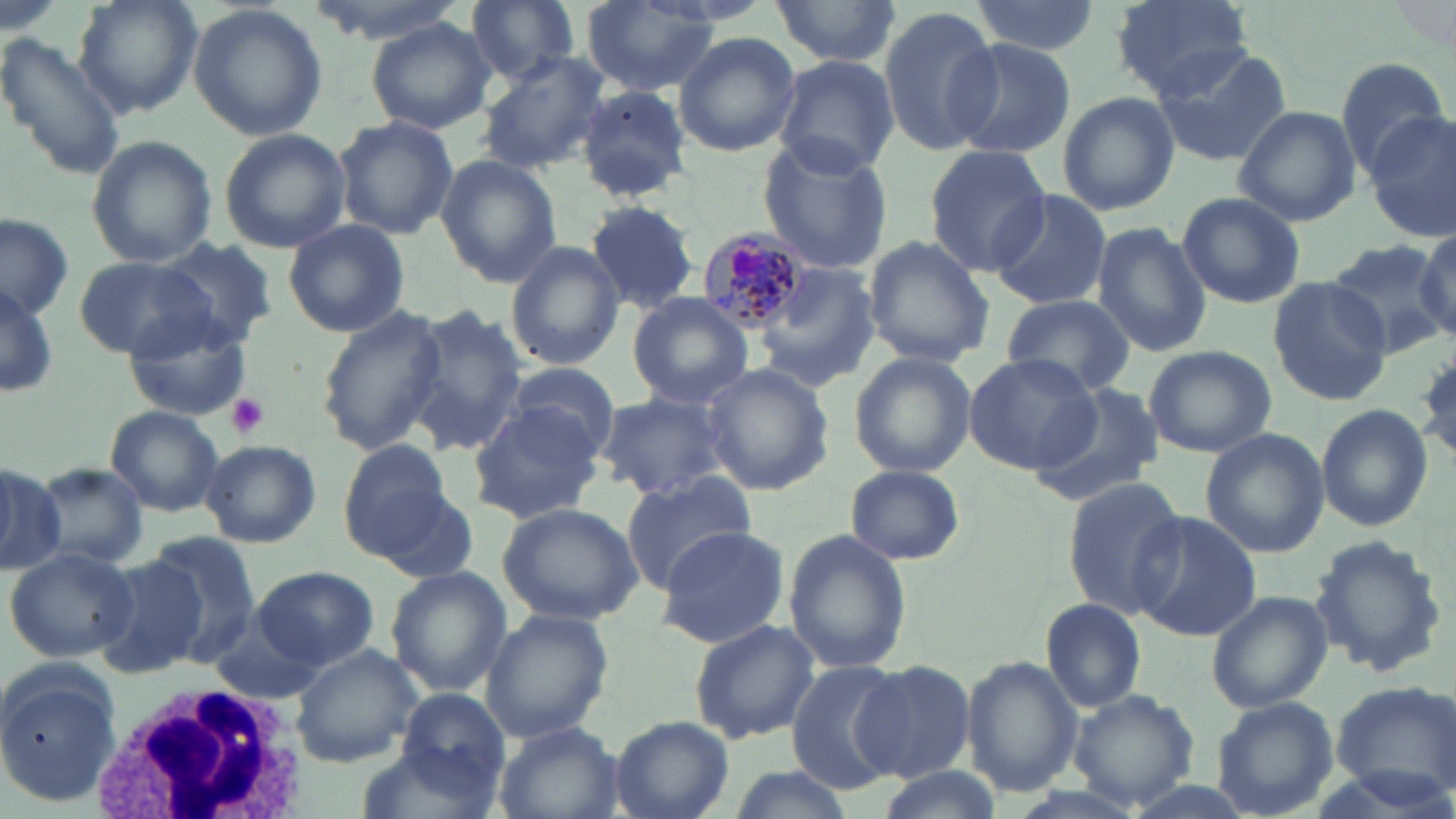
Approximate bounding boxes as [x1, y1, x2, y2] in pixels. Uninfected red blood cell locations: [73, 0, 202, 117], [766, 0, 903, 70], [969, 0, 1100, 56], [1110, 1, 1253, 98], [464, 2, 580, 84], [580, 2, 726, 97], [187, 3, 329, 142], [877, 5, 1000, 157], [366, 18, 496, 135], [0, 32, 127, 179], [672, 32, 801, 158], [943, 37, 1076, 161], [1153, 39, 1289, 169], [478, 45, 609, 177], [771, 55, 900, 178], [1332, 56, 1449, 176], [574, 86, 694, 203], [1058, 92, 1178, 216], [1233, 105, 1361, 226], [1365, 112, 1455, 240], [331, 116, 459, 241], [219, 127, 349, 252], [85, 135, 217, 268], [757, 138, 895, 273], [925, 146, 1055, 274], [435, 155, 562, 286], [987, 190, 1114, 312], [1176, 192, 1306, 309], [583, 201, 699, 313], [0, 216, 75, 324], [282, 219, 410, 338], [1091, 222, 1211, 357], [1413, 227, 1456, 341], [862, 235, 994, 367], [155, 237, 280, 346], [1322, 239, 1454, 358], [504, 241, 625, 370], [74, 256, 217, 359], [759, 263, 881, 391], [1267, 278, 1396, 404], [0, 282, 58, 399], [626, 293, 756, 408], [999, 295, 1136, 398], [316, 304, 449, 456], [399, 305, 528, 456], [123, 309, 255, 421], [1142, 344, 1275, 458], [849, 352, 976, 477], [966, 354, 1100, 472], [502, 362, 620, 460], [698, 364, 836, 497], [1032, 383, 1166, 506], [594, 390, 735, 502], [466, 401, 604, 523], [106, 405, 225, 516], [1315, 405, 1433, 531], [1200, 429, 1328, 557], [199, 439, 321, 547], [337, 439, 455, 558], [0, 463, 63, 572], [31, 463, 152, 572], [845, 464, 965, 563], [618, 471, 756, 592], [1059, 476, 1187, 618], [367, 477, 479, 584], [496, 501, 646, 624], [1129, 510, 1261, 641], [656, 524, 791, 648], [784, 531, 910, 674], [146, 532, 260, 655], [1308, 533, 1450, 678], [4, 546, 140, 663], [95, 556, 209, 678], [386, 566, 512, 695], [254, 567, 379, 669], [1206, 590, 1330, 712], [1037, 599, 1147, 713], [479, 608, 614, 741], [688, 618, 820, 744], [208, 619, 330, 705], [290, 643, 423, 767], [962, 655, 1083, 799], [854, 660, 977, 783], [789, 662, 910, 794], [0, 665, 121, 803], [1330, 679, 1456, 800], [1067, 688, 1201, 811], [397, 689, 509, 790], [1207, 697, 1340, 819], [611, 717, 734, 819], [490, 723, 626, 819], [353, 745, 501, 818], [870, 763, 1001, 819]. Platelet locations: [225, 393, 271, 437]. White blood cell locations: [84, 682, 309, 818]. Plasmodium malariae-infected red blood cell locations: [694, 224, 816, 333]. Slide-level diagnosis: Plasmodium malariae. Optical microscopy. One field of a larger specimen. Image is 1456×819 pixels. May-Grünwald-Giemsa stain. Thin blood film. Captured at 1000x magnification.